Locate every cell, classifying each as a parasitized red blood cell, an uninfected red blood cell, or a white blood cell.
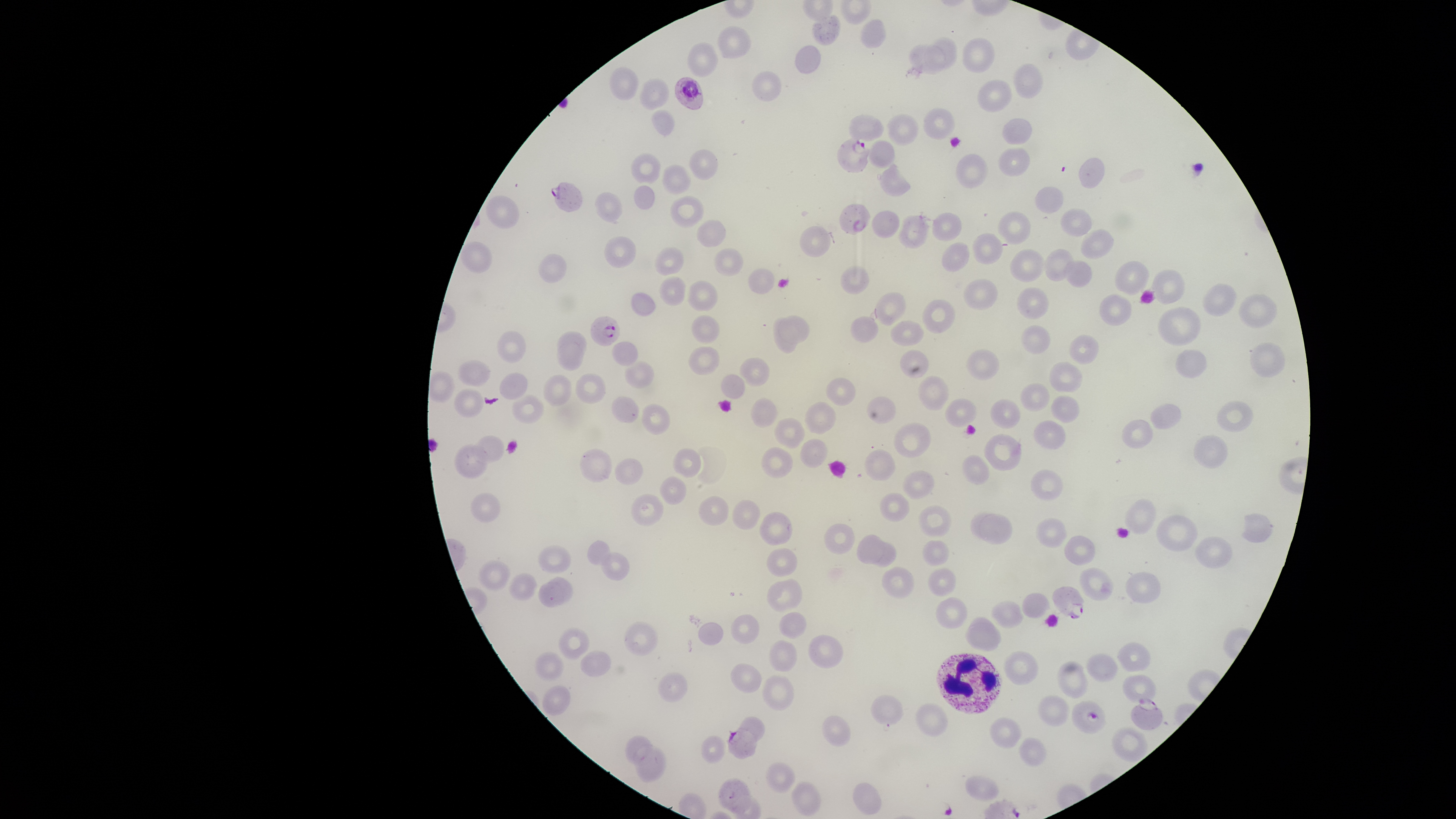

Approximate bounding boxes, in pixels from the top-left corner.
Parasitized red blood cells: (left=674, top=76, right=704, bottom=111), (left=837, top=136, right=873, bottom=174), (left=550, top=182, right=583, bottom=212), (left=839, top=203, right=871, bottom=236), (left=590, top=316, right=620, bottom=346), (left=1051, top=585, right=1085, bottom=620), (left=1130, top=699, right=1164, bottom=730), (left=1072, top=700, right=1107, bottom=733), (left=726, top=727, right=757, bottom=759).
Uninfected red blood cells: (left=811, top=14, right=841, bottom=46), (left=859, top=18, right=887, bottom=49), (left=717, top=25, right=752, bottom=59), (left=924, top=36, right=958, bottom=70), (left=961, top=37, right=995, bottom=73), (left=686, top=41, right=719, bottom=78), (left=907, top=43, right=946, bottom=74), (left=794, top=44, right=822, bottom=73), (left=1012, top=63, right=1043, bottom=100), (left=609, top=67, right=639, bottom=100), (left=751, top=70, right=782, bottom=102), (left=639, top=77, right=669, bottom=111), (left=977, top=79, right=1013, bottom=113), (left=923, top=107, right=955, bottom=139), (left=651, top=109, right=676, bottom=136), (left=886, top=113, right=919, bottom=145), (left=848, top=114, right=884, bottom=141), (left=1002, top=117, right=1033, bottom=145), (left=867, top=140, right=895, bottom=168), (left=997, top=147, right=1030, bottom=177), (left=689, top=149, right=719, bottom=180), (left=630, top=152, right=662, bottom=184), (left=955, top=154, right=989, bottom=189), (left=1077, top=158, right=1106, bottom=188), (left=877, top=163, right=911, bottom=197), (left=662, top=164, right=692, bottom=194), (left=634, top=184, right=655, bottom=209), (left=1034, top=186, right=1064, bottom=214), (left=594, top=191, right=623, bottom=223), (left=485, top=195, right=520, bottom=229), (left=669, top=195, right=704, bottom=228), (left=1060, top=208, right=1093, bottom=237), (left=871, top=210, right=900, bottom=239), (left=997, top=211, right=1032, bottom=245), (left=931, top=212, right=962, bottom=242), (left=897, top=214, right=931, bottom=249), (left=696, top=220, right=726, bottom=248), (left=799, top=225, right=831, bottom=258), (left=1080, top=228, right=1114, bottom=259), (left=972, top=233, right=1003, bottom=264), (left=603, top=236, right=636, bottom=268), (left=460, top=242, right=492, bottom=273), (left=941, top=243, right=970, bottom=272), (left=655, top=247, right=684, bottom=276), (left=713, top=247, right=744, bottom=276), (left=1044, top=248, right=1076, bottom=281), (left=1009, top=249, right=1045, bottom=282), (left=537, top=253, right=567, bottom=283), (left=1063, top=260, right=1093, bottom=287), (left=1114, top=260, right=1149, bottom=295), (left=840, top=266, right=869, bottom=294), (left=748, top=268, right=775, bottom=294), (left=1150, top=268, right=1186, bottom=305), (left=659, top=276, right=686, bottom=306), (left=962, top=278, right=998, bottom=309), (left=687, top=280, right=719, bottom=311), (left=1203, top=282, right=1237, bottom=316), (left=1016, top=287, right=1050, bottom=320), (left=631, top=291, right=657, bottom=315), (left=872, top=292, right=907, bottom=326), (left=1238, top=292, right=1277, bottom=328), (left=1099, top=293, right=1131, bottom=326), (left=922, top=299, right=955, bottom=334), (left=1157, top=305, right=1202, bottom=346), (left=691, top=314, right=720, bottom=344), (left=777, top=315, right=811, bottom=343), (left=850, top=315, right=878, bottom=343), (left=772, top=316, right=797, bottom=353), (left=889, top=320, right=924, bottom=347), (left=1020, top=324, right=1051, bottom=355), (left=557, top=330, right=588, bottom=360), (left=496, top=331, right=527, bottom=363), (left=1068, top=334, right=1100, bottom=364), (left=610, top=340, right=639, bottom=367), (left=557, top=341, right=584, bottom=371), (left=1248, top=341, right=1287, bottom=379), (left=688, top=346, right=720, bottom=376), (left=899, top=348, right=929, bottom=378), (left=965, top=348, right=1000, bottom=381), (left=1174, top=348, right=1207, bottom=378), (left=739, top=357, right=770, bottom=387), (left=457, top=360, right=491, bottom=386), (left=625, top=360, right=655, bottom=390), (left=1049, top=361, right=1083, bottom=394), (left=500, top=372, right=528, bottom=400), (left=575, top=373, right=607, bottom=404), (left=543, top=374, right=571, bottom=406), (left=720, top=374, right=746, bottom=398), (left=825, top=376, right=857, bottom=406), (left=918, top=376, right=949, bottom=410), (left=1020, top=382, right=1050, bottom=412), (left=454, top=388, right=484, bottom=417), (left=511, top=395, right=544, bottom=424), (left=1050, top=395, right=1080, bottom=424), (left=611, top=396, right=639, bottom=423), (left=866, top=396, right=897, bottom=424), (left=944, top=397, right=977, bottom=428), (left=750, top=398, right=779, bottom=428), (left=990, top=398, right=1021, bottom=429), (left=804, top=401, right=836, bottom=434), (left=1216, top=401, right=1253, bottom=433), (left=1150, top=402, right=1182, bottom=429), (left=642, top=403, right=670, bottom=435), (left=774, top=416, right=807, bottom=447), (left=1121, top=417, right=1153, bottom=449), (left=1034, top=420, right=1067, bottom=450), (left=893, top=423, right=931, bottom=458), (left=983, top=433, right=1022, bottom=470), (left=472, top=434, right=506, bottom=464), (left=1193, top=435, right=1227, bottom=468), (left=799, top=438, right=828, bottom=469), (left=454, top=443, right=490, bottom=478), (left=760, top=446, right=794, bottom=478), (left=579, top=448, right=613, bottom=482), (left=673, top=448, right=701, bottom=479), (left=864, top=449, right=896, bottom=481), (left=962, top=455, right=990, bottom=485), (left=614, top=457, right=643, bottom=485), (left=1030, top=469, right=1062, bottom=501), (left=902, top=470, right=934, bottom=500), (left=658, top=476, right=687, bottom=505), (left=471, top=492, right=500, bottom=524), (left=879, top=492, right=909, bottom=522), (left=631, top=493, right=665, bottom=527), (left=697, top=495, right=730, bottom=526), (left=1124, top=498, right=1157, bottom=534), (left=732, top=499, right=761, bottom=530), (left=918, top=505, right=952, bottom=538), (left=759, top=511, right=793, bottom=546), (left=969, top=512, right=1013, bottom=545), (left=1240, top=513, right=1275, bottom=542), (left=1156, top=514, right=1198, bottom=552), (left=1036, top=517, right=1068, bottom=548), (left=823, top=523, right=855, bottom=555), (left=856, top=533, right=884, bottom=565), (left=1064, top=535, right=1096, bottom=566), (left=1195, top=535, right=1234, bottom=569), (left=587, top=539, right=613, bottom=565), (left=922, top=539, right=949, bottom=567), (left=868, top=540, right=897, bottom=568), (left=538, top=544, right=572, bottom=574), (left=766, top=547, right=798, bottom=577), (left=601, top=552, right=630, bottom=581), (left=477, top=559, right=511, bottom=591), (left=882, top=567, right=915, bottom=599), (left=928, top=567, right=957, bottom=596), (left=1078, top=567, right=1114, bottom=601), (left=508, top=572, right=538, bottom=601), (left=1125, top=572, right=1161, bottom=604), (left=548, top=576, right=573, bottom=603), (left=767, top=578, right=803, bottom=613), (left=537, top=580, right=564, bottom=609), (left=1021, top=592, right=1050, bottom=618), (left=935, top=597, right=968, bottom=630), (left=990, top=600, right=1025, bottom=628), (left=778, top=612, right=807, bottom=639), (left=730, top=614, right=760, bottom=644), (left=964, top=617, right=1001, bottom=651), (left=623, top=621, right=659, bottom=656), (left=698, top=621, right=725, bottom=645), (left=558, top=627, right=590, bottom=660), (left=807, top=634, right=844, bottom=669), (left=768, top=639, right=798, bottom=672), (left=1117, top=642, right=1151, bottom=672), (left=534, top=650, right=565, bottom=681), (left=579, top=650, right=612, bottom=677), (left=1004, top=650, right=1039, bottom=685), (left=1086, top=652, right=1118, bottom=683), (left=1057, top=661, right=1088, bottom=699), (left=730, top=662, right=763, bottom=693), (left=658, top=671, right=688, bottom=702), (left=762, top=674, right=794, bottom=711), (left=1122, top=674, right=1156, bottom=702), (left=542, top=685, right=571, bottom=716), (left=869, top=694, right=904, bottom=727), (left=1037, top=695, right=1070, bottom=727), (left=915, top=702, right=948, bottom=737), (left=820, top=715, right=852, bottom=747), (left=989, top=716, right=1023, bottom=749), (left=738, top=717, right=765, bottom=743), (left=1110, top=728, right=1148, bottom=763), (left=625, top=735, right=653, bottom=766), (left=700, top=735, right=726, bottom=764), (left=1019, top=737, right=1047, bottom=767), (left=633, top=744, right=667, bottom=782), (left=765, top=762, right=796, bottom=794), (left=965, top=775, right=999, bottom=802), (left=718, top=777, right=752, bottom=813), (left=791, top=781, right=821, bottom=817), (left=852, top=782, right=882, bottom=815).
White blood cells: (left=935, top=653, right=1003, bottom=714).

The visible region is circular. Giemsa stain. Species: Plasmodium falciparum. Photographed with a smartphone camera through the microscope eyepiece. Single field of view. Thin blood smear. Image is 1456×819 pixels.